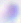 Toxoplasma gondii is shown. Micrograph. 400x magnification.